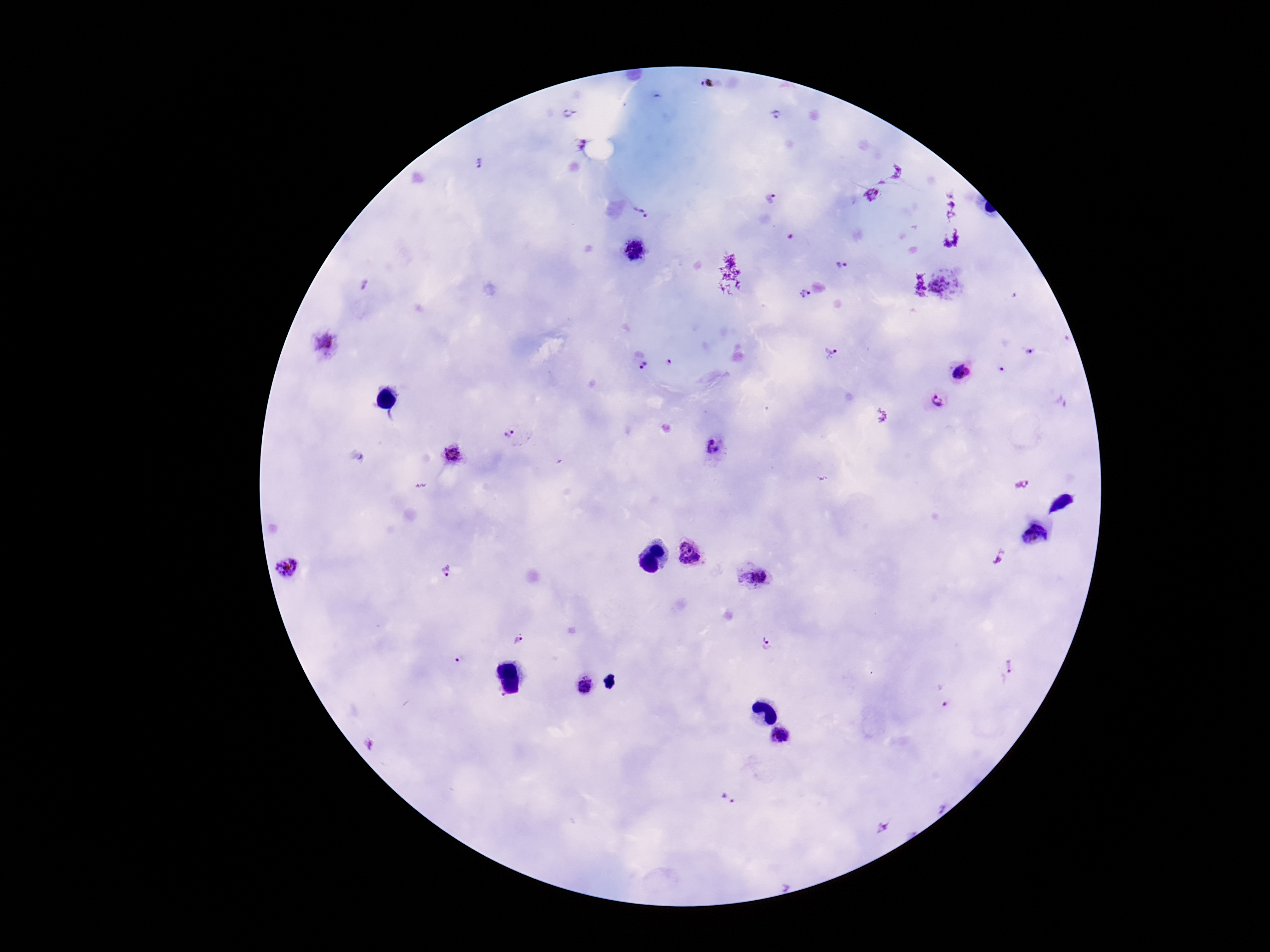
Approximate centers as [x, y] in pixels.
Summary:
  - Plasmodium parasite locations: [569, 114], [775, 116], [577, 144], [479, 162], [770, 198], [642, 213], [636, 252], [842, 266], [941, 284], [366, 285], [805, 293], [327, 348], [832, 351], [1031, 351], [669, 363], [643, 367], [1003, 369], [962, 372], [938, 401], [513, 437], [715, 449], [451, 454], [689, 554], [287, 567], [446, 572], [753, 579], [519, 641], [768, 643], [461, 660], [1009, 669], [586, 686], [779, 735], [729, 799]
  - Patient malaria status: infected
  - Field of view: one from this slide
  - Preparation: thick blood smear
  - Magnification: 100x
  - Stain: Giemsa
  - Image size: 1270×952 pixels
  - Capture: smartphone camera through the microscope eyepiece